State which parasite is depicted.
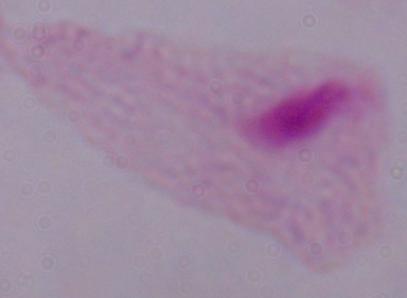
This is a trichomonad.

modality: photomicrograph
magnification: 1000x